Identify the preparation type.
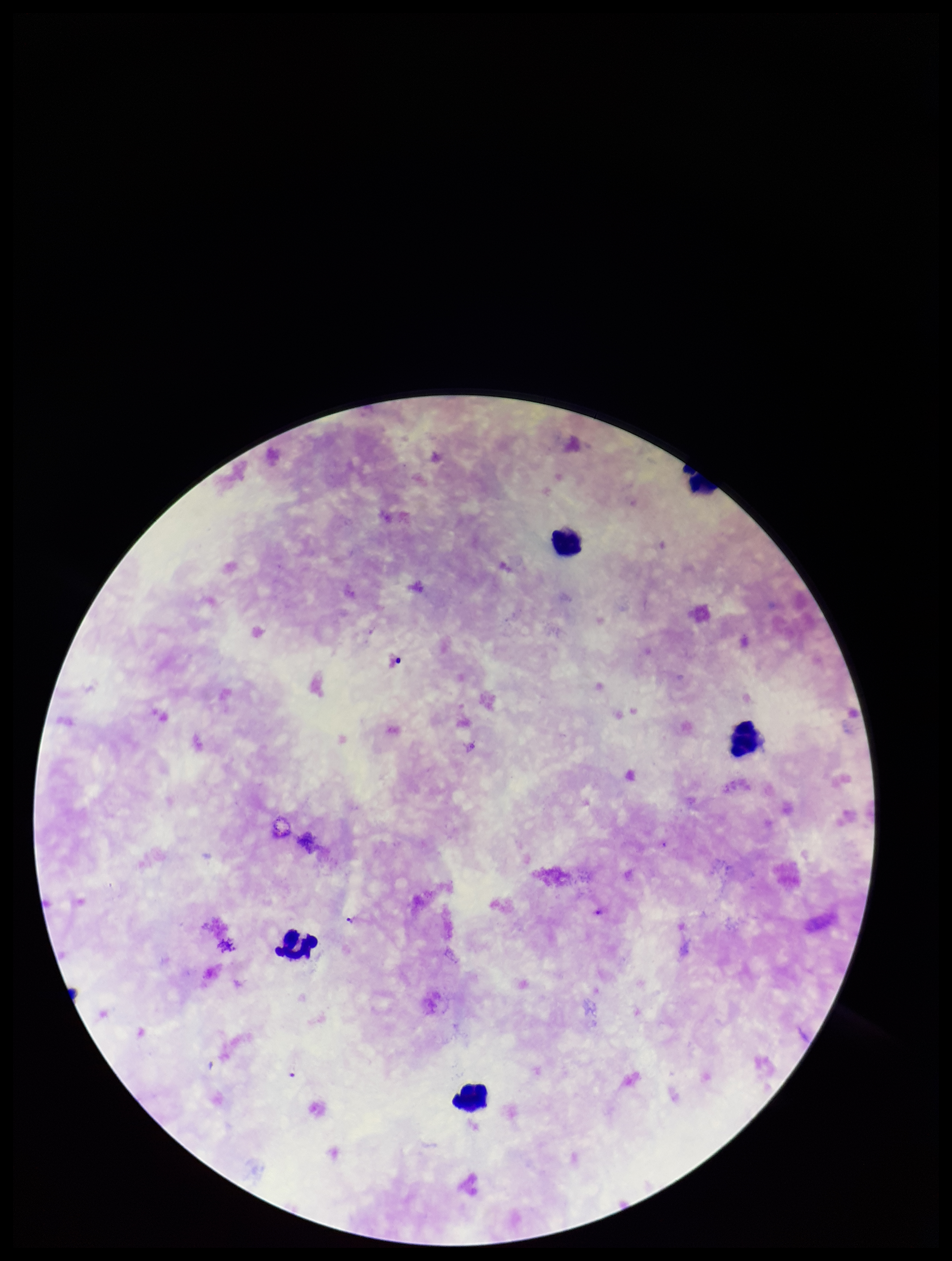
A thick smear.

stain = Giemsa
patient malaria status = infected
parasite count = 3
image size = 952×1261 pixels
Plasmodium parasites = seen
leukocyte count = 4
field of view = one from this slide
capture = smartphone photograph through the microscope eyepiece
species reported for this patient = Plasmodium falciparum